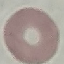
Result: no malaria parasites detected. Giemsa stain. Cell patch, automatically extracted from a larger field of view and resized to 64 × 64 pixels. Acquired by smartphone through the microscope eyepiece. Thin blood smear.